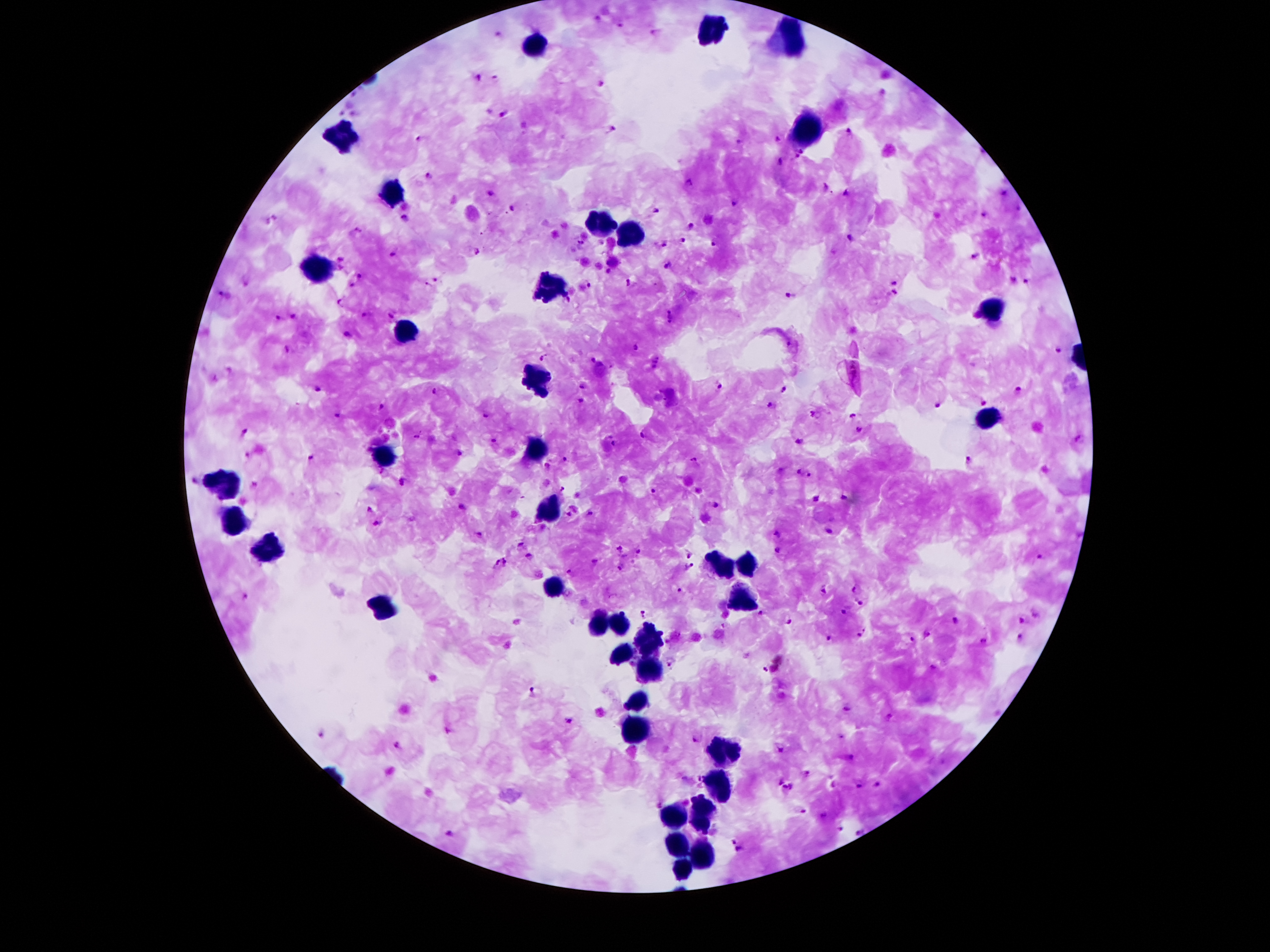

Approximate centers as {x, y} in pixels.
Summary:
  - Leukocyte locations: {712, 30}, {791, 38}, {535, 43}, {804, 131}, {344, 134}, {394, 190}, {602, 225}, {630, 236}, {317, 269}, {550, 288}, {993, 311}, {409, 335}, {539, 382}, {989, 419}, {535, 450}, {388, 456}, {218, 484}, {550, 511}, {235, 524}, {270, 551}, {722, 562}, {745, 566}, {554, 587}, {743, 601}, {384, 608}, {596, 619}, {619, 623}, {644, 644}, {619, 654}, {646, 669}, {638, 703}, {636, 730}, {724, 753}, {716, 791}, {697, 814}, {674, 822}, {678, 848}, {703, 853}, {682, 871}
  - Plasmodium parasite locations: {597, 18}, {623, 25}, {498, 34}, {657, 35}, {475, 76}, {496, 78}, {600, 85}, {487, 112}, {503, 114}, {611, 129}, {850, 133}, {419, 138}, {778, 139}, {738, 143}, {799, 150}, {794, 158}, {780, 163}, {431, 176}, {689, 183}, {826, 188}, {846, 192}, {493, 193}, {1004, 194}, {733, 204}, {512, 210}, {1017, 210}, {658, 211}, {983, 216}, {405, 221}, {689, 228}, {354, 232}, {851, 239}, {682, 242}, {580, 243}, {664, 244}, {715, 244}, {475, 251}, {393, 254}, {977, 257}, {340, 260}, {613, 262}, {668, 266}, {339, 272}, {608, 274}, {361, 277}, {438, 281}, {1012, 281}, {893, 282}, {1026, 282}, {631, 283}, {588, 286}, {895, 293}, {224, 296}, {791, 296}, {340, 303}, {567, 303}, {366, 316}, {391, 316}, {672, 317}, {294, 318}, {278, 319}, {348, 335}, {635, 346}, {287, 347}, {1057, 351}, {543, 356}, {594, 360}, {656, 364}, {856, 368}, {213, 379}, {583, 386}, {718, 386}, {317, 391}, {783, 391}, {433, 392}, {1020, 392}, {579, 400}, {983, 401}, {770, 405}, {381, 406}, {936, 406}, {814, 414}, {338, 416}, {485, 416}, {854, 417}, {858, 430}, {244, 433}, {642, 434}, {416, 436}, {1078, 439}, {493, 440}, {799, 442}, {613, 443}, {460, 453}, {246, 457}, {310, 458}, {565, 459}, {696, 462}, {969, 462}, {547, 466}, {796, 472}, {810, 476}, {196, 481}, {401, 482}, {561, 488}, {652, 491}, {844, 497}, {812, 498}, {573, 507}, {716, 507}, {460, 508}, {369, 510}, {589, 515}, {569, 517}, {377, 525}, {828, 531}, {776, 532}, {479, 535}, {521, 544}, {620, 550}, {639, 552}, {779, 553}, {689, 556}, {527, 557}, {1038, 559}, {507, 561}, {494, 562}, {594, 563}, {621, 568}, {688, 569}, {569, 571}, {857, 588}, {682, 591}, {826, 591}, {246, 599}, {859, 603}, {844, 612}, {760, 613}, {1032, 614}, {642, 615}, {1019, 619}, {954, 621}, {788, 622}, {861, 634}, {1018, 637}, {829, 640}, {910, 642}, {984, 643}, {671, 663}, {931, 668}, {765, 670}, {530, 693}, {848, 709}, {889, 718}, {570, 721}, {320, 734}, {842, 737}, {696, 740}, {398, 746}, {779, 751}, {851, 757}, {806, 773}, {778, 780}, {692, 781}, {878, 784}, {792, 786}, {861, 787}, {783, 791}, {800, 810}, {823, 817}, {841, 829}, {857, 832}, {450, 834}, {738, 846}
  - Patient malaria status: infected with Plasmodium falciparum
  - Capture: smartphone through the microscope eyepiece
  - Stain: Giemsa
  - Magnification: 100x
  - Field of view: single
  - Preparation: thick blood smear
  - Image size: 1270×952 pixels